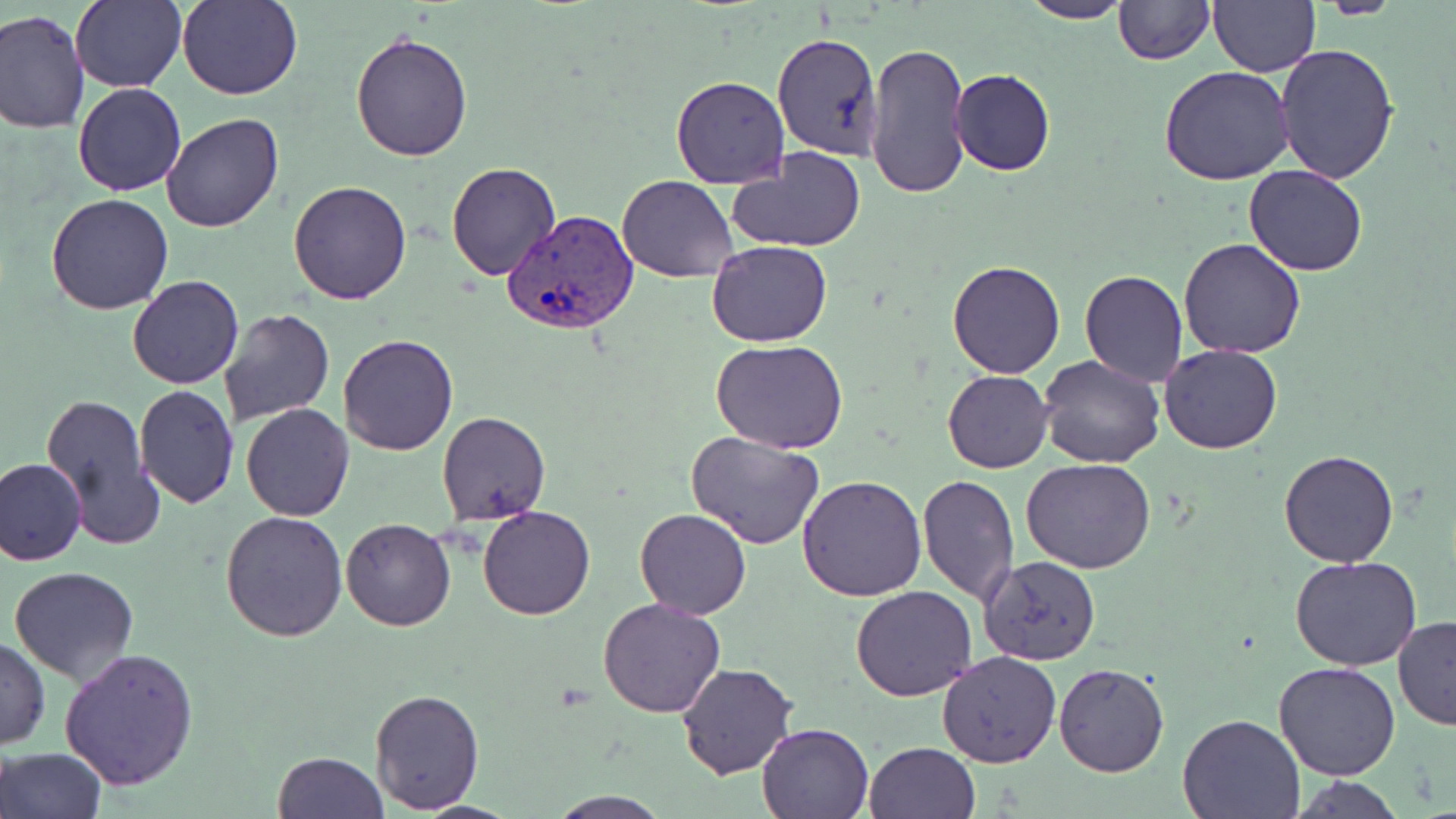 Approximate bounding boxes as (x1, y1, x2, y2) in pixels. Plasmodium vivax-infected red blood cell locations: (503, 210, 640, 334). Uninfected red blood cell locations: (69, 0, 187, 91), (177, 0, 304, 101), (1018, 0, 1135, 24), (1114, 0, 1214, 64), (1208, 0, 1320, 77), (1315, 0, 1404, 19), (0, 10, 90, 134), (772, 30, 885, 161), (350, 31, 473, 160), (867, 41, 971, 201), (1274, 41, 1400, 185), (1157, 65, 1297, 185), (950, 69, 1055, 176), (670, 75, 791, 189), (73, 82, 186, 197), (161, 112, 284, 233), (728, 146, 867, 253), (445, 162, 560, 281), (1245, 164, 1366, 277), (617, 175, 739, 282), (288, 179, 414, 304), (45, 193, 175, 315), (1178, 237, 1306, 360), (706, 240, 834, 347), (946, 259, 1065, 379), (1079, 269, 1189, 387), (128, 275, 245, 390), (217, 307, 336, 427), (337, 333, 459, 456), (711, 339, 848, 455), (1159, 344, 1283, 455), (1038, 355, 1166, 471), (943, 370, 1053, 473), (134, 383, 240, 506), (39, 392, 163, 548), (135, 394, 351, 512), (241, 403, 353, 520), (1050, 407, 1169, 536), (437, 411, 550, 526), (684, 431, 825, 549), (1279, 449, 1398, 567), (1, 458, 87, 566), (1021, 458, 1154, 574), (916, 473, 1020, 606), (797, 476, 928, 601), (477, 504, 595, 620), (635, 509, 751, 618), (220, 512, 349, 643), (339, 517, 456, 630), (979, 555, 1101, 665), (1291, 557, 1423, 672), (9, 566, 139, 684), (851, 585, 977, 701), (597, 596, 726, 717), (1392, 615, 1456, 730), (0, 635, 50, 750), (59, 648, 199, 790), (936, 651, 1062, 769), (676, 662, 798, 780), (1274, 662, 1402, 780), (1053, 663, 1169, 778), (370, 687, 484, 812), (1177, 713, 1306, 819), (756, 721, 876, 818), (862, 741, 981, 819), (1, 747, 105, 819), (272, 752, 387, 818), (1291, 776, 1406, 818), (549, 792, 672, 819). Slide-level diagnosis: Plasmodium vivax. May-Grünwald-Giemsa stain. Light microscopy. Image is 1456×819 pixels. 1000x magnification. Thin blood film. Single field of view.